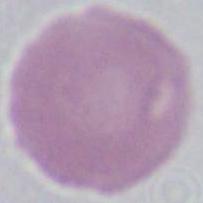
Summary:
  - Modality: photomicrograph
  - Magnification: 1000x
  - Identification: erythrocyte